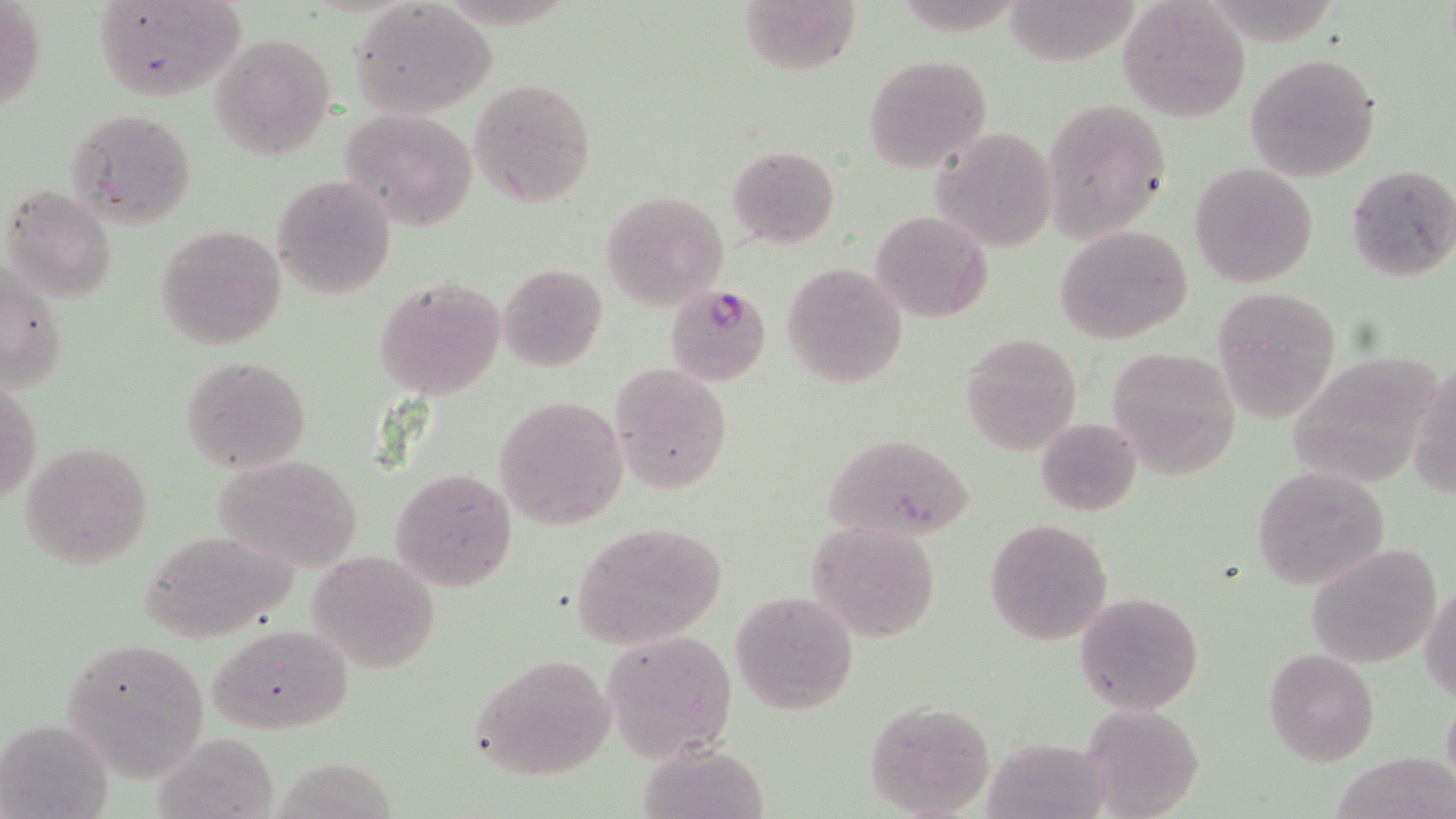
Summary:
  - Coordinate format: approximate bounding boxes as named x1/y1/x2/y2 corners in pixels
  - Uninfected red blood cell locations: (x1=0, y1=0, x2=46, y2=116), (x1=92, y1=1, x2=246, y2=105), (x1=736, y1=1, x2=863, y2=80), (x1=1118, y1=2, x2=1251, y2=122), (x1=350, y1=3, x2=498, y2=117), (x1=1004, y1=4, x2=1144, y2=68), (x1=213, y1=32, x2=334, y2=159), (x1=1245, y1=53, x2=1382, y2=180), (x1=863, y1=54, x2=992, y2=174), (x1=469, y1=77, x2=597, y2=208), (x1=1041, y1=97, x2=1171, y2=242), (x1=341, y1=106, x2=478, y2=231), (x1=66, y1=108, x2=196, y2=228), (x1=929, y1=125, x2=1059, y2=253), (x1=726, y1=143, x2=840, y2=249), (x1=1189, y1=163, x2=1318, y2=288), (x1=1346, y1=163, x2=1456, y2=283), (x1=272, y1=175, x2=397, y2=299), (x1=2, y1=184, x2=117, y2=302), (x1=601, y1=190, x2=728, y2=310), (x1=871, y1=210, x2=992, y2=321), (x1=155, y1=224, x2=287, y2=352), (x1=1052, y1=225, x2=1195, y2=345), (x1=2, y1=255, x2=69, y2=391), (x1=781, y1=260, x2=909, y2=387), (x1=498, y1=262, x2=607, y2=372), (x1=376, y1=277, x2=506, y2=399), (x1=1212, y1=287, x2=1345, y2=420), (x1=960, y1=332, x2=1085, y2=455), (x1=1106, y1=347, x2=1242, y2=480), (x1=1283, y1=351, x2=1439, y2=484), (x1=179, y1=354, x2=314, y2=474), (x1=1411, y1=361, x2=1456, y2=501), (x1=611, y1=363, x2=734, y2=494), (x1=2, y1=375, x2=40, y2=507), (x1=495, y1=395, x2=628, y2=529), (x1=1034, y1=416, x2=1142, y2=517), (x1=819, y1=431, x2=979, y2=542), (x1=22, y1=439, x2=152, y2=569), (x1=213, y1=453, x2=365, y2=572), (x1=390, y1=465, x2=518, y2=594), (x1=1249, y1=465, x2=1391, y2=591), (x1=983, y1=518, x2=1114, y2=645), (x1=570, y1=520, x2=729, y2=652), (x1=807, y1=520, x2=942, y2=642), (x1=136, y1=526, x2=300, y2=646), (x1=1305, y1=543, x2=1441, y2=666), (x1=307, y1=549, x2=441, y2=675), (x1=1421, y1=584, x2=1455, y2=700), (x1=730, y1=591, x2=859, y2=715), (x1=1075, y1=591, x2=1203, y2=714), (x1=205, y1=623, x2=352, y2=735), (x1=601, y1=627, x2=738, y2=761), (x1=59, y1=637, x2=209, y2=781), (x1=1264, y1=649, x2=1379, y2=766), (x1=469, y1=653, x2=618, y2=781), (x1=865, y1=699, x2=996, y2=818), (x1=1078, y1=706, x2=1206, y2=816), (x1=1, y1=715, x2=114, y2=819), (x1=151, y1=729, x2=272, y2=816), (x1=983, y1=739, x2=1117, y2=819), (x1=1327, y1=752, x2=1456, y2=819), (x1=276, y1=759, x2=408, y2=819)
  - Plasmodium falciparum-infected red blood cell locations: (x1=664, y1=283, x2=772, y2=387)
  - Slide-level diagnosis: Plasmodium falciparum
  - Magnification: 1000x
  - Stain: May-Grünwald-Giemsa
  - Preparation: thin blood film
  - Image size: 1456×819 pixels
  - Field of view: one of a larger specimen
  - Modality: light microscopy